Report the malaria status of this cell.
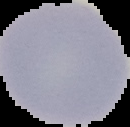

Uninfected.

Summary:
  - Image size: 130×127 pixels
  - Preparation: thin blood film
  - Image type: segmented cell region on a black background